Assess this cell for malaria.
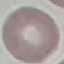
Uninfected.

Summary:
  - Image type: cell patch, automatically extracted from a larger field of view and resized to 64 × 64 pixels
  - Preparation: thin blood film
  - Stain: Giemsa
  - Capture: smartphone camera at the microscope eyepiece